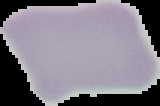
image type = segmented cell region on a black background
result = no Plasmodium parasites detected
preparation = thin blood smear
image size = 160×106 pixels